Locate every malaria parasite by life-cycle stage, and every leukocyte.
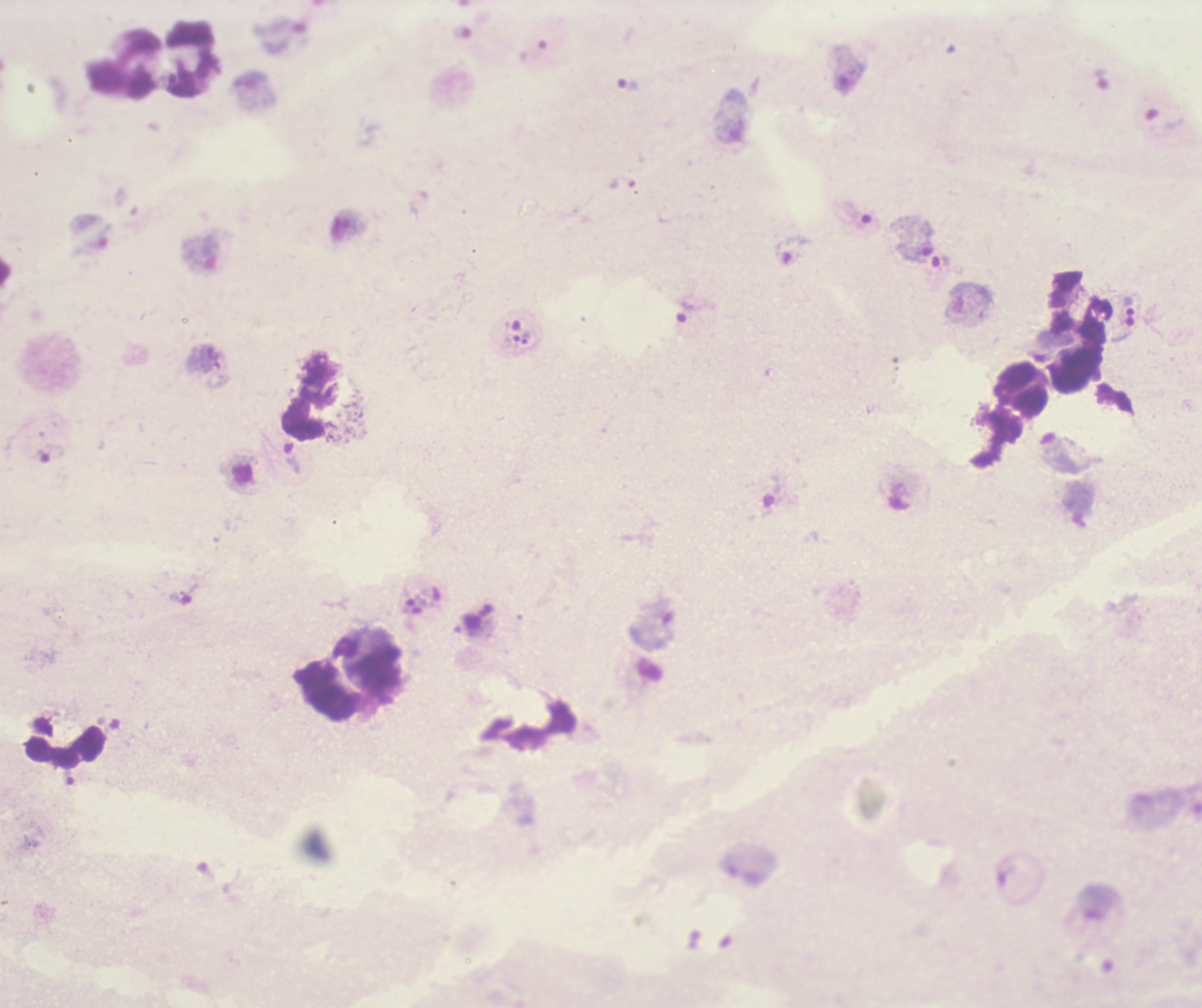

Approximate centers as {x, y} in pixels.
Trophozoites: {629, 85}, {1129, 306}, {686, 312}, {526, 338}, {50, 454}.
No schizont or gametocyte forms observed.
Leukocytes: {123, 65}, {1022, 389}, {66, 747}.

{
  "magnification": "100x",
  "coloration_quality": "bad",
  "field_of_view": "single",
  "background_quality": "unsatisfactory",
  "stain": "Romanowsky",
  "preparation": "thick blood smear",
  "image_size": "1202×1008 pixels",
  "context": "previously used in a real diagnosis"
}